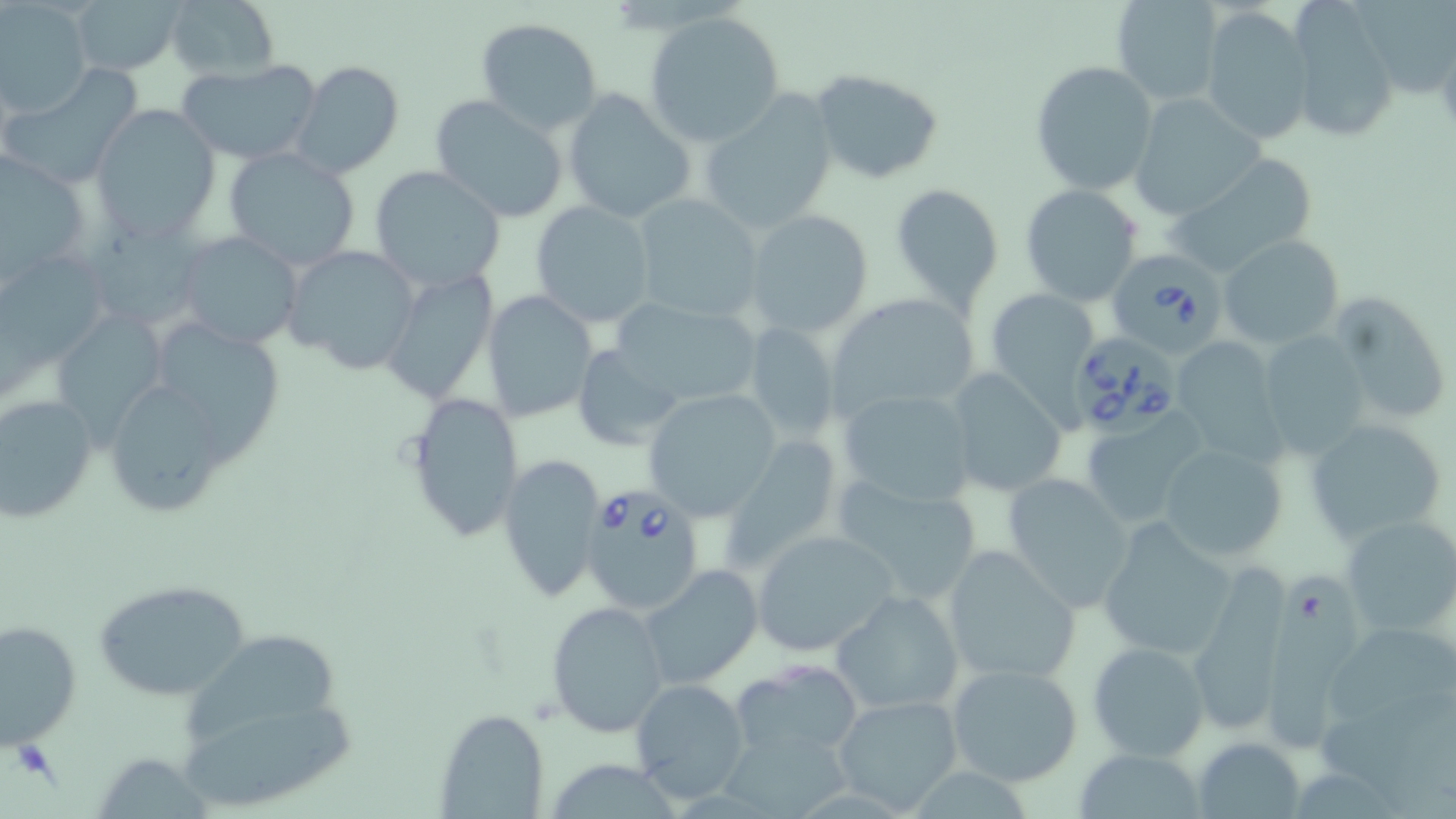
Babesia divergens-infected red blood cell locations = approximate bounding boxes as [x1, y1, x2, y2] in pixels: [1104, 251, 1225, 356], [1069, 329, 1183, 437], [581, 488, 705, 617]
slide-level diagnosis = Babesia divergens
field of view = one of a larger specimen
modality = light microscopy
preparation = thin blood smear
magnification = 1000x
uninfected red blood cell locations = approximate bounding boxes as [x1, y1, x2, y2] in pixels: [67, 0, 182, 75], [164, 0, 279, 83], [1111, 0, 1226, 106], [1349, 0, 1456, 104], [0, 3, 93, 115], [1285, 3, 1400, 143], [1198, 7, 1313, 145], [644, 11, 786, 147], [474, 17, 603, 134], [175, 58, 321, 166], [292, 59, 405, 179], [1030, 61, 1159, 196], [809, 68, 947, 186], [2, 69, 142, 180], [560, 89, 697, 223], [430, 93, 571, 223], [699, 93, 840, 230], [1129, 94, 1264, 219], [93, 106, 220, 239], [222, 147, 363, 271], [0, 152, 97, 286], [1166, 152, 1322, 277], [369, 164, 505, 292], [889, 182, 1005, 309], [1019, 185, 1143, 306], [630, 193, 766, 322], [530, 200, 656, 327], [744, 209, 874, 337], [85, 213, 221, 337], [176, 231, 306, 349], [1219, 235, 1344, 347], [283, 244, 422, 376], [0, 254, 124, 406], [380, 269, 499, 405], [1329, 289, 1453, 427], [985, 290, 1098, 418], [481, 291, 597, 422], [825, 293, 981, 420], [606, 295, 764, 413], [57, 302, 180, 445], [165, 318, 288, 477], [743, 321, 840, 443], [1257, 330, 1372, 458], [1170, 337, 1281, 459], [571, 347, 689, 447], [945, 367, 1069, 498], [98, 371, 241, 521], [835, 386, 980, 508], [643, 389, 781, 522], [403, 391, 523, 544], [0, 395, 98, 523], [1079, 417, 1204, 526], [1306, 419, 1445, 545], [1155, 442, 1289, 563], [499, 452, 605, 601], [1003, 472, 1135, 607], [832, 473, 986, 606], [1340, 515, 1456, 639], [1098, 520, 1237, 659], [752, 529, 898, 657], [940, 545, 1080, 686], [1185, 559, 1292, 738], [640, 563, 764, 687], [1258, 568, 1380, 748], [93, 578, 251, 700], [833, 590, 965, 712], [546, 600, 669, 738], [0, 616, 83, 746], [1331, 622, 1456, 718], [172, 629, 346, 746], [1087, 640, 1209, 762], [731, 659, 863, 763], [946, 662, 1084, 788], [628, 679, 750, 804], [831, 693, 965, 815], [180, 699, 367, 816], [434, 708, 548, 818], [725, 733, 852, 819], [1195, 735, 1306, 818], [1077, 749, 1210, 819], [552, 753, 673, 819], [101, 757, 215, 819]
image size = 1456×819 pixels
stain = May-Grünwald-Giemsa